State which cell type is depicted.
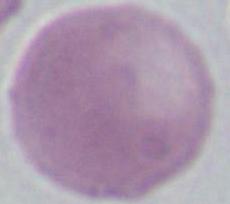

An erythrocyte.

magnification = 1000x
modality = photomicrograph